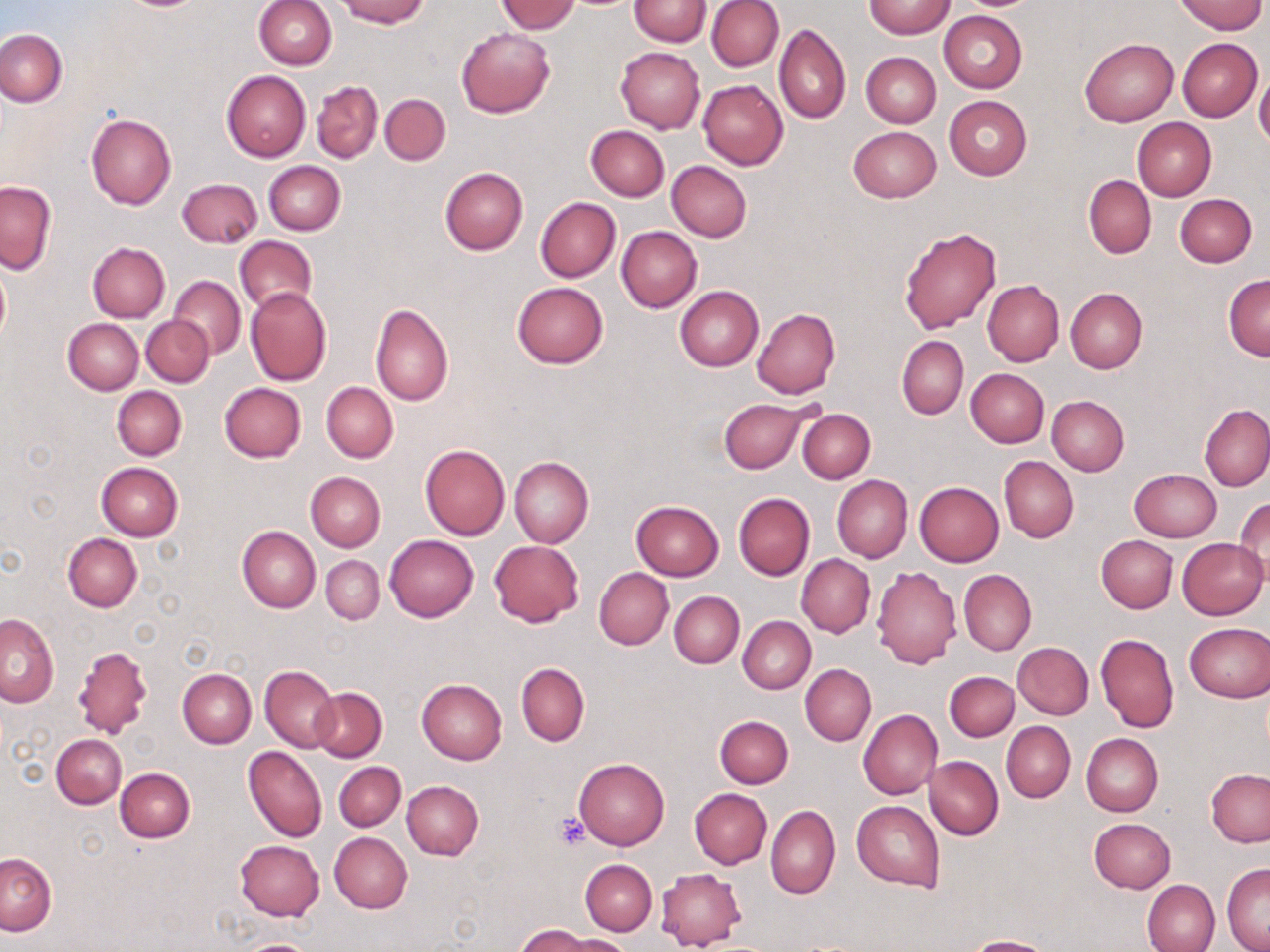

Summary:
  - Coordinate format: approximate bounding boxes as [x1, y1, x2, y2] in pixels
  - Platelet locations: [554, 814, 591, 849]
  - Uninfected red blood cell locations: [338, 0, 428, 27], [628, 0, 712, 46], [706, 0, 783, 72], [1176, 0, 1265, 35], [253, 1, 336, 68], [497, 1, 580, 34], [864, 1, 955, 39], [938, 11, 1027, 92], [775, 23, 851, 125], [456, 27, 554, 117], [0, 28, 66, 107], [1079, 38, 1178, 126], [1178, 38, 1262, 121], [616, 47, 705, 133], [861, 52, 940, 127], [1254, 69, 1270, 151], [221, 70, 310, 162], [698, 80, 788, 169], [312, 81, 383, 163], [380, 94, 450, 165], [944, 95, 1032, 180], [86, 112, 176, 209], [1132, 119, 1216, 199], [585, 125, 669, 201], [847, 126, 940, 203], [263, 160, 346, 235], [666, 161, 752, 241], [439, 167, 528, 255], [1083, 175, 1156, 258], [177, 178, 262, 248], [0, 180, 55, 275], [1174, 193, 1257, 267], [535, 197, 620, 282], [898, 225, 1001, 334], [615, 226, 702, 313], [233, 234, 316, 316], [87, 242, 170, 322], [0, 265, 10, 343], [1223, 274, 1270, 360], [169, 276, 245, 358], [982, 279, 1064, 365], [511, 281, 608, 369], [675, 286, 763, 371], [245, 287, 331, 386], [1065, 288, 1147, 373], [369, 303, 454, 406], [752, 308, 840, 399], [142, 315, 214, 387], [63, 317, 143, 395], [896, 336, 968, 419], [965, 368, 1049, 447], [321, 381, 398, 463], [219, 382, 306, 462], [112, 386, 187, 460], [1046, 395, 1129, 476], [719, 398, 809, 475], [1200, 404, 1269, 491], [797, 408, 875, 482], [419, 443, 509, 541], [999, 456, 1078, 542], [509, 458, 593, 548], [95, 463, 183, 541], [1129, 469, 1221, 541], [306, 471, 385, 552], [832, 475, 912, 563], [913, 482, 1003, 567], [733, 493, 814, 580], [1234, 498, 1270, 583], [631, 500, 724, 581], [237, 525, 320, 612], [63, 533, 142, 613], [384, 534, 478, 622], [1096, 535, 1178, 612], [1176, 537, 1268, 620], [489, 540, 583, 627], [797, 555, 875, 637], [321, 556, 384, 625], [871, 565, 962, 668], [594, 567, 673, 650], [958, 570, 1036, 656], [670, 591, 743, 667], [0, 614, 59, 707], [738, 617, 815, 693], [1183, 621, 1269, 702], [1096, 633, 1178, 734], [1013, 642, 1094, 719], [71, 644, 153, 739], [516, 663, 589, 746], [800, 664, 875, 746], [260, 665, 339, 753], [177, 668, 256, 748], [945, 672, 1019, 741], [417, 679, 507, 764], [310, 688, 387, 761], [858, 709, 942, 799], [714, 715, 793, 788], [1001, 721, 1075, 803], [1081, 733, 1163, 816], [51, 734, 126, 808], [244, 746, 328, 843], [925, 755, 1003, 839], [574, 757, 669, 850], [334, 762, 406, 831], [115, 768, 195, 843], [1206, 768, 1270, 847], [402, 781, 483, 860], [689, 788, 772, 869], [852, 801, 944, 890], [766, 805, 840, 899], [1089, 818, 1176, 893], [328, 831, 412, 914], [234, 840, 325, 920], [1, 853, 56, 936], [580, 859, 656, 935], [1222, 863, 1270, 952], [657, 868, 746, 950], [1142, 879, 1220, 952], [516, 923, 606, 951], [551, 934, 633, 952], [963, 935, 1055, 952], [236, 938, 323, 952]
  - Slide-level diagnosis: no evidence of blood parasites
  - Stain: May-Grünwald-Giemsa
  - Image size: 1270×952 pixels
  - Preparation: thin blood film
  - Magnification: 1000x
  - Field of view: one of a larger specimen
  - Modality: optical microscopy